Classify this cell by malaria status.
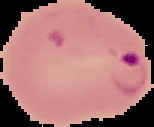
It is parasitized.

From a thin blood smear. Cell region segmented out of the field of view; the surrounding area is masked to black. Image is 154×127 pixels.